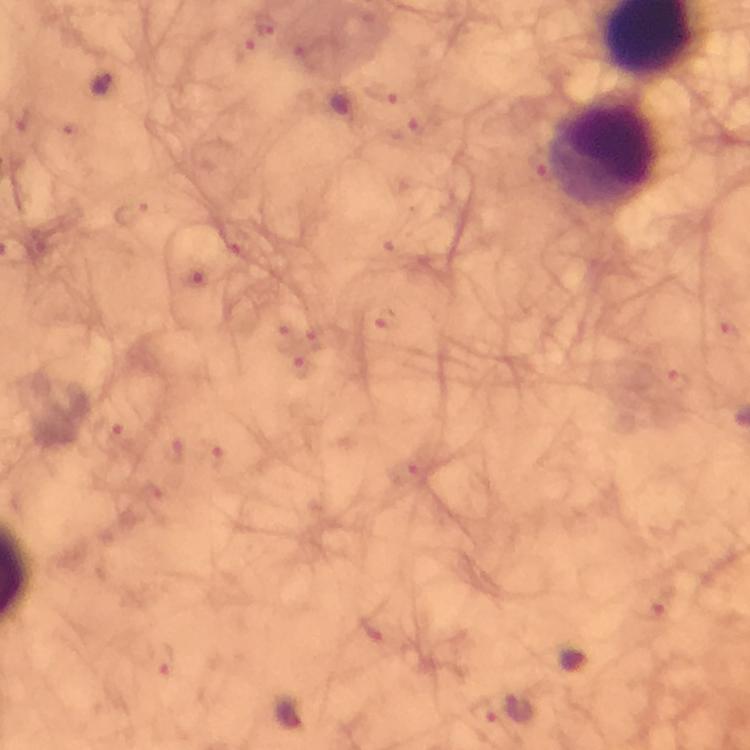
magnification = 100x
leukocyte locations = approximate centers as [x, y] in pixels: [607, 153]
cropped from = a single field of view
stain = Giemsa
context = from a malaria diagnostic workup
image size = 750×750 pixels
immersion oil = applied
Plasmodium parasite locations = approximate centers as [x, y] in pixels: [103, 85], [287, 713]
capture = smartphone camera through the microscope
preparation = thick smear